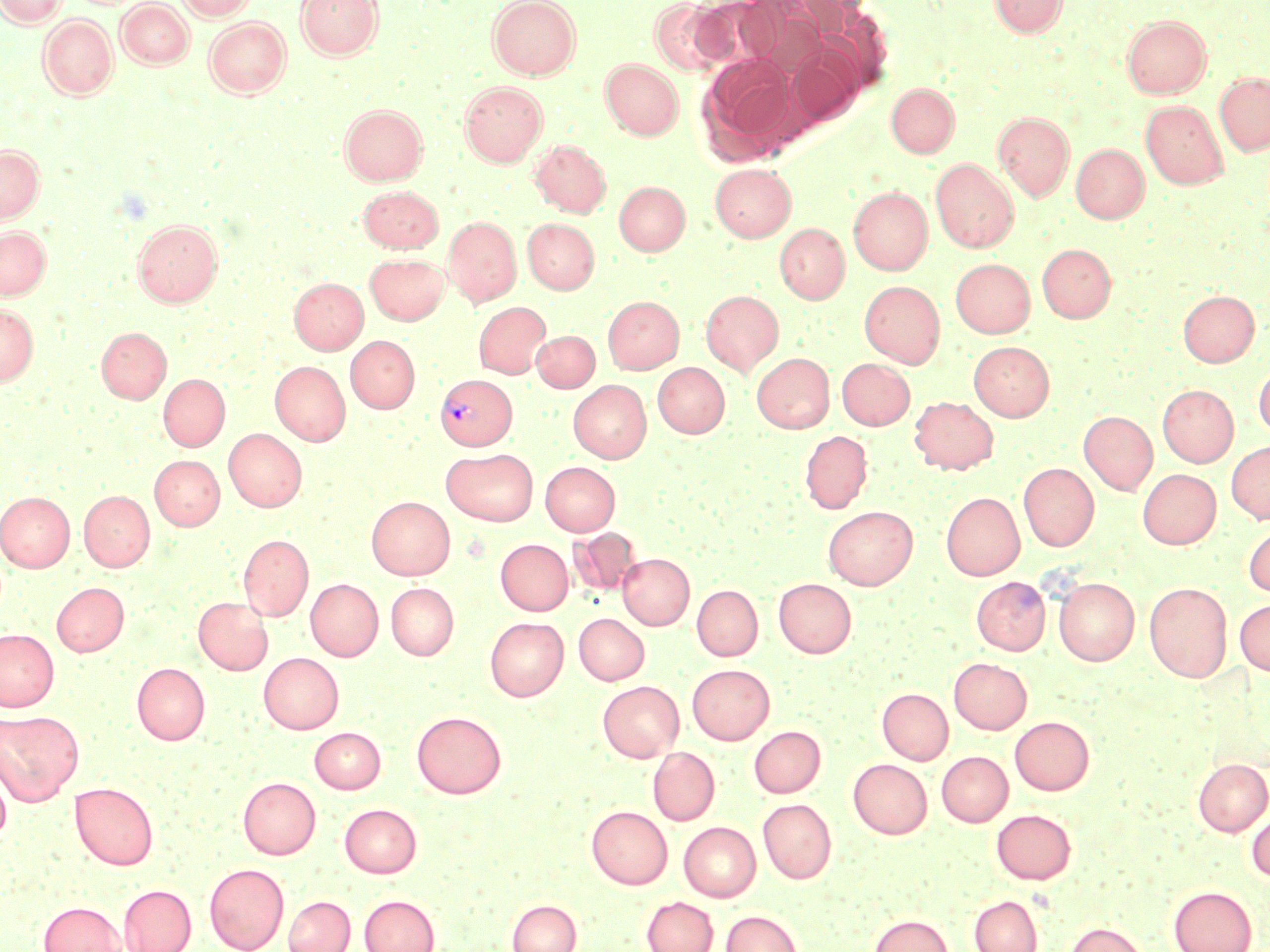
slide-level diagnosis = Plasmodium vivax
field of view = single
image size = 1270×952 pixels
uninfected red blood cell locations = approximate bounding boxes as [x1, y1, x2, y2] in pixels: [0, 0, 66, 27], [176, 0, 256, 20], [296, 0, 383, 59], [488, 0, 581, 80], [649, 0, 731, 75], [692, 0, 778, 69], [989, 0, 1067, 37], [117, 1, 193, 68], [38, 15, 118, 99], [1122, 15, 1211, 98], [203, 16, 291, 97], [789, 47, 861, 124], [698, 55, 800, 160], [601, 59, 683, 139], [1215, 72, 1270, 155], [459, 80, 547, 166], [886, 83, 960, 157], [1140, 100, 1228, 189], [339, 104, 427, 184], [993, 112, 1074, 200], [530, 140, 611, 217], [1071, 143, 1149, 223], [0, 144, 44, 224], [931, 159, 1018, 252], [710, 163, 796, 241], [614, 181, 690, 254], [358, 184, 443, 252], [849, 187, 932, 274], [443, 216, 521, 305], [522, 218, 599, 293], [132, 219, 222, 307], [775, 223, 849, 303], [0, 226, 50, 299], [1037, 243, 1115, 322], [365, 253, 449, 324], [951, 259, 1034, 337], [289, 277, 368, 354], [860, 280, 945, 367], [701, 290, 783, 375], [1178, 290, 1259, 367], [603, 295, 683, 373], [0, 301, 39, 386], [474, 302, 550, 378], [97, 327, 171, 403], [532, 330, 599, 392], [345, 336, 419, 412], [969, 341, 1054, 420], [752, 353, 834, 432], [837, 358, 914, 430], [270, 361, 350, 445], [653, 362, 730, 437], [1254, 363, 1270, 438], [158, 374, 229, 450], [568, 380, 651, 462], [1157, 384, 1238, 466], [910, 396, 998, 474], [1079, 411, 1157, 493], [224, 428, 306, 511], [800, 430, 872, 513], [1226, 440, 1270, 524], [441, 449, 538, 525], [150, 455, 224, 530], [541, 461, 620, 535], [1019, 463, 1099, 550], [1137, 468, 1221, 549], [79, 490, 154, 571], [0, 492, 74, 572], [941, 492, 1024, 580], [367, 496, 454, 579], [823, 506, 917, 589], [1243, 522, 1270, 596], [567, 528, 642, 598], [239, 534, 313, 620], [496, 539, 573, 615], [618, 553, 694, 629], [971, 576, 1050, 654], [1054, 577, 1139, 665], [306, 578, 383, 660], [774, 578, 856, 658], [52, 582, 129, 656], [386, 582, 458, 660], [1144, 582, 1233, 682], [692, 584, 762, 660], [193, 596, 273, 674], [1235, 598, 1270, 676], [574, 613, 649, 685], [485, 617, 568, 700], [0, 629, 58, 711], [258, 652, 343, 733], [949, 657, 1032, 734], [132, 663, 209, 744], [687, 664, 774, 744], [598, 680, 683, 761], [878, 688, 953, 764], [0, 710, 83, 805], [411, 711, 506, 798], [1010, 716, 1094, 794], [749, 725, 825, 797], [310, 726, 385, 793], [648, 747, 719, 826], [936, 750, 1013, 827], [1193, 758, 1270, 835], [848, 759, 932, 838], [0, 767, 11, 844], [238, 776, 320, 858], [70, 782, 158, 869], [758, 798, 836, 883], [339, 803, 421, 877], [587, 806, 672, 888], [991, 808, 1076, 884], [1247, 809, 1270, 883], [679, 821, 760, 901], [204, 862, 289, 952], [118, 884, 195, 952], [1169, 885, 1256, 952], [360, 894, 439, 952], [283, 895, 355, 952], [969, 895, 1043, 952], [642, 897, 718, 952], [507, 899, 581, 952], [38, 901, 126, 952], [721, 910, 803, 952], [869, 913, 953, 952], [1064, 922, 1148, 952]
stain = May-Grünwald-Giemsa
preparation = thin blood smear
modality = optical microscopy
magnification = 1000x
Plasmodium vivax-infected red blood cell locations = approximate bounding boxes as [x1, y1, x2, y2] in pixels: [437, 375, 518, 452]